Look for Plasmodium parasites.
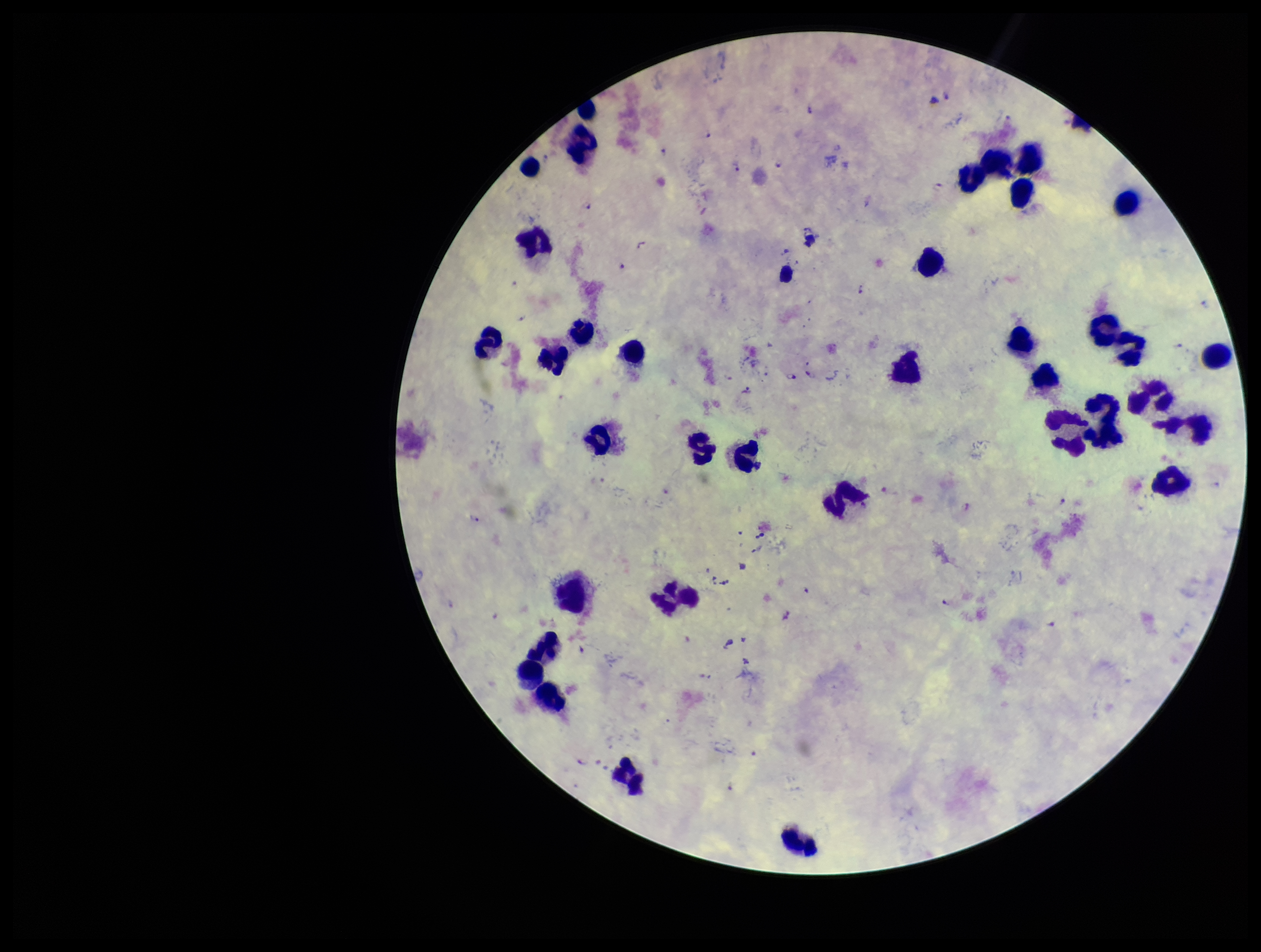
Identified.

Parasite count: 20. Photographed through the microscope eyepiece with a smartphone camera. Preparation: thick blood smear. Species reported for this patient: Plasmodium falciparum. Single field of view. Patient malaria status: infected. Image is 1261×952 pixels. Stained with Giemsa. Leukocyte count: 35.